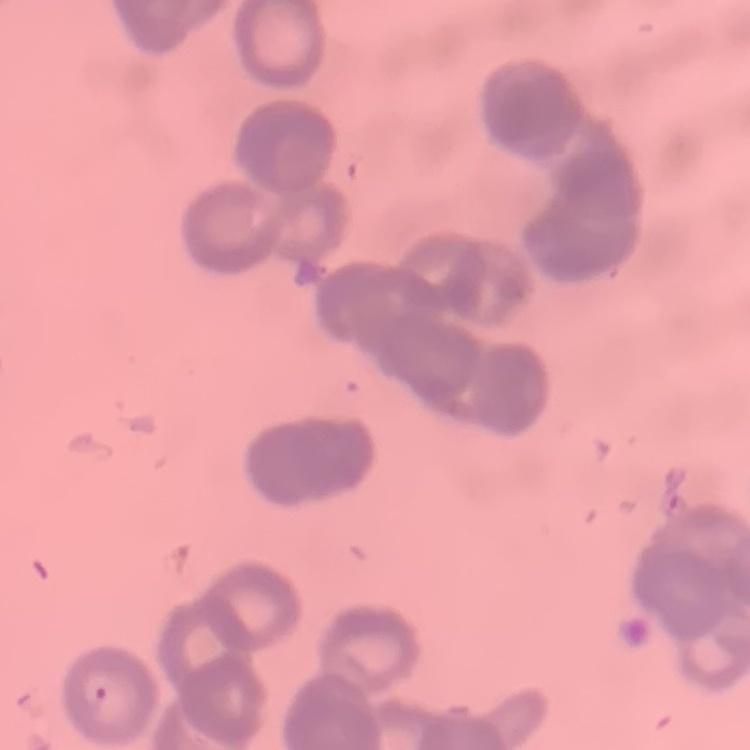 The red blood cells show rouleaux formation. Square crop of a larger photomicrograph. Field's or Giemsa stain. Thin peripheral smear.